Assess this cell for malaria.
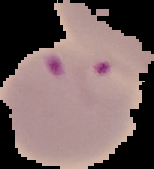
It is parasitized.

The area outside the segmented cell region is set to black. From a thin blood film. Image is 154×169 pixels.